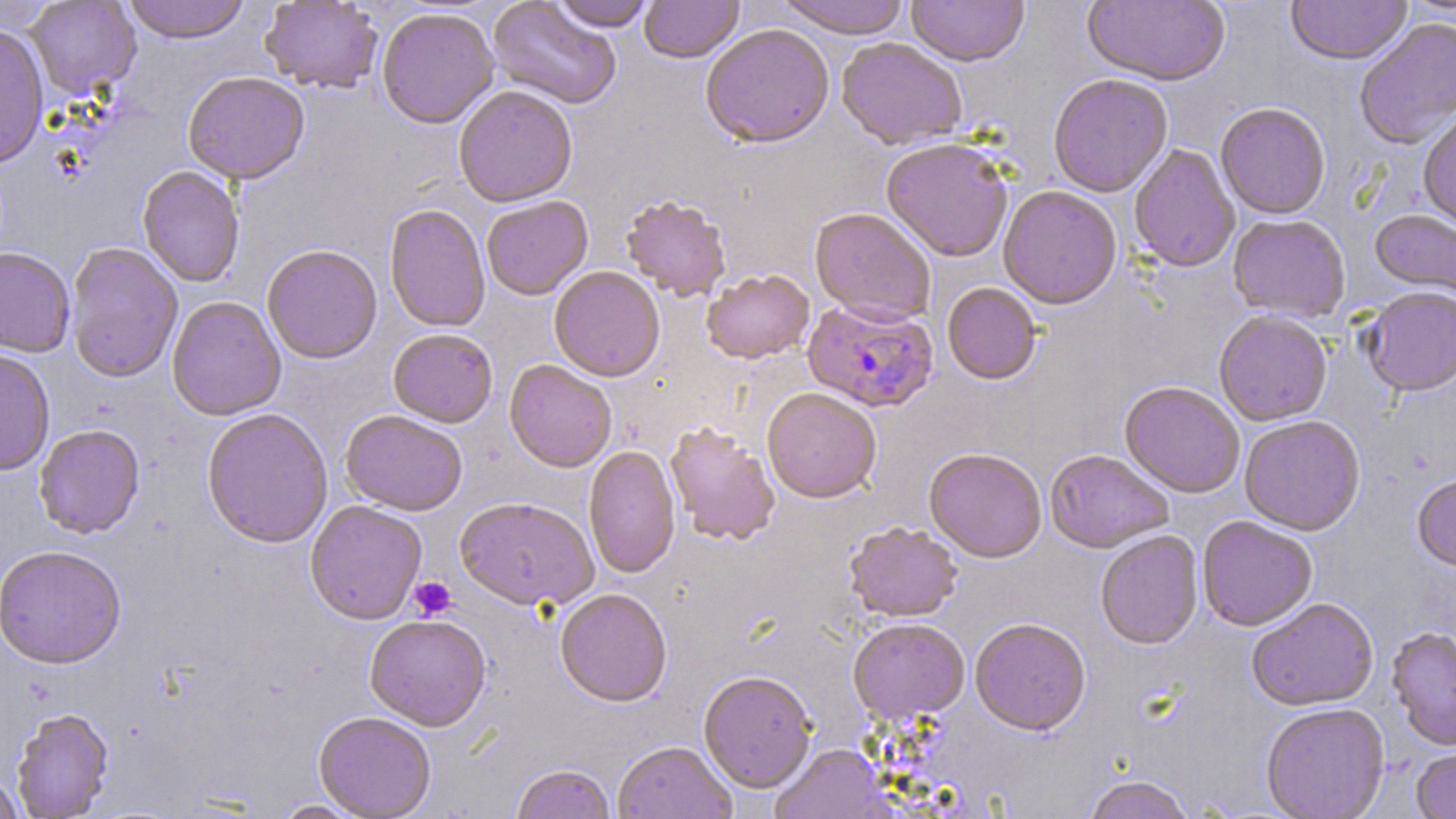
Summary:
  - Coordinate format: approximate bounding boxes as (x1,y1)-(x2,y2) corner pairs in pixels
  - Uninfected red blood cell locations: (24,0)-(141,99), (122,0)-(251,44), (487,0)-(622,110), (639,0)-(743,64), (775,0)-(911,39), (907,0)-(1029,67), (1083,0)-(1231,87), (1285,0)-(1412,66), (260,1)-(383,94), (550,1)-(656,32), (376,7)-(500,129), (1354,18)-(1456,151), (0,23)-(50,169), (699,23)-(835,149), (836,37)-(968,151), (182,71)-(310,185), (1048,74)-(1173,197), (453,85)-(578,208), (1215,103)-(1330,219), (1418,110)-(1456,231), (881,137)-(1013,263), (1129,144)-(1240,273), (137,166)-(245,288), (998,185)-(1122,309), (620,194)-(732,302), (481,196)-(593,300), (384,204)-(490,333), (810,208)-(936,326), (1369,209)-(1456,303), (1228,214)-(1350,322), (65,242)-(183,383), (262,245)-(382,364), (0,247)-(76,358), (549,266)-(665,382), (701,270)-(814,365), (942,282)-(1042,385), (1360,287)-(1456,397), (167,295)-(286,421), (1213,310)-(1332,426), (388,328)-(498,428), (0,349)-(55,476), (504,360)-(617,473), (1119,382)-(1245,499), (762,388)-(882,504), (201,408)-(333,549), (341,410)-(467,516), (1239,416)-(1365,536), (664,423)-(781,546), (34,424)-(145,539), (583,446)-(681,579), (924,448)-(1047,563), (1045,449)-(1174,553), (1412,473)-(1456,572), (454,497)-(598,612), (305,500)-(427,625), (1196,516)-(1318,631), (844,521)-(962,623), (1095,531)-(1203,650), (1,545)-(127,670), (555,589)-(673,707), (1247,598)-(1378,711), (364,615)-(491,731), (847,618)-(969,724), (970,619)-(1090,736), (1387,626)-(1456,752), (698,671)-(817,794), (1261,703)-(1390,819), (11,708)-(114,819), (313,712)-(436,818), (613,741)-(737,819), (771,744)-(893,818), (1411,747)-(1456,819), (511,765)-(615,819), (0,772)-(25,819), (1082,775)-(1196,819), (272,799)-(370,818)
  - Platelet locations: (410,576)-(457,620)
  - Plasmodium falciparum-infected red blood cell locations: (802,299)-(939,413)
  - Slide-level diagnosis: Plasmodium falciparum
  - Field of view: one of a larger specimen
  - Preparation: thin blood film
  - Modality: light microscopy
  - Magnification: 1000x
  - Image size: 1456×819 pixels
  - Stain: May-Grünwald-Giemsa